Outline each blood parasite and name the species.
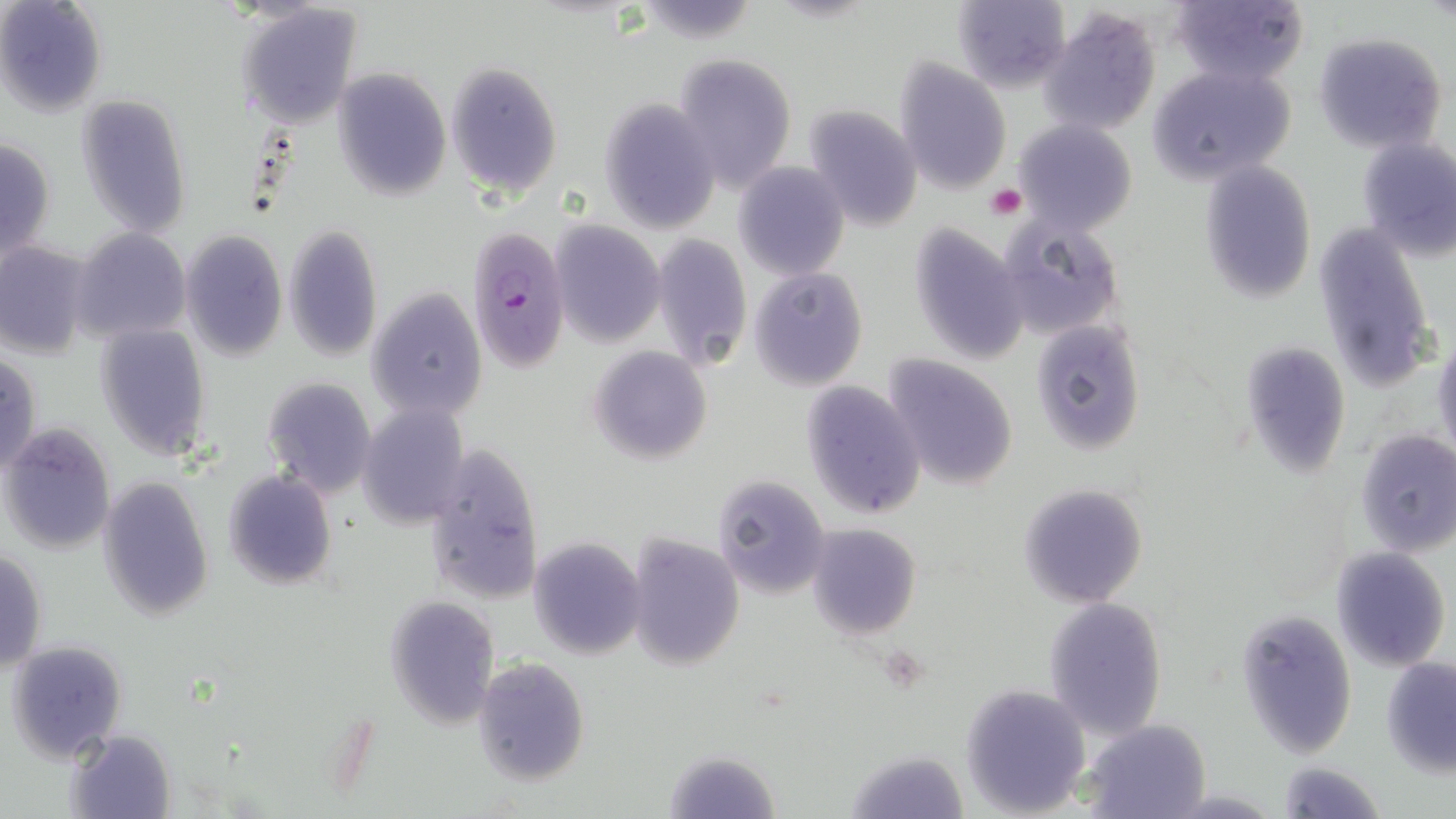

Approximate bounding boxes as (x1, y1, x2, y2) in pixels.
Plasmodium falciparum-infected red blood cells: (465, 223, 572, 370).
No Plasmodium ovale, Plasmodium malariae, Plasmodium vivax, Babesia divergens, or Trypanosoma brucei observed.

slide-level diagnosis = Plasmodium falciparum
field of view = single
preparation = thin blood film
modality = light microscopy
stain = May-Grünwald-Giemsa
uninfected red blood cell locations = approximate bounding boxes as (x1, y1, x2, y2) in pixels: (0, 0, 106, 116), (953, 0, 1071, 94), (1170, 0, 1309, 88), (237, 3, 363, 127), (1040, 9, 1161, 136), (1312, 32, 1447, 152), (673, 53, 797, 192), (894, 60, 1011, 195), (445, 61, 563, 197), (1149, 62, 1299, 185), (331, 68, 450, 201), (75, 96, 191, 237), (599, 100, 723, 233), (802, 106, 922, 229), (1012, 120, 1137, 236), (0, 137, 56, 262), (1356, 137, 1456, 262), (1198, 160, 1318, 305), (734, 163, 850, 280), (1002, 219, 1123, 334), (549, 222, 665, 347), (908, 222, 1030, 366), (1314, 225, 1437, 396), (285, 226, 384, 361), (72, 229, 191, 342), (180, 231, 288, 360), (652, 234, 753, 371), (0, 241, 92, 359), (749, 267, 868, 390), (365, 290, 487, 422), (1028, 321, 1146, 455), (95, 324, 211, 460), (1433, 332, 1456, 464), (1240, 342, 1352, 479), (587, 346, 713, 465), (0, 353, 42, 477), (882, 353, 1019, 490), (261, 376, 376, 499), (800, 380, 926, 521), (360, 402, 471, 527), (1, 424, 116, 555), (1356, 429, 1456, 558), (423, 445, 544, 606), (223, 469, 337, 590), (98, 474, 213, 619), (712, 474, 833, 598), (1017, 483, 1148, 608), (805, 523, 921, 641), (624, 533, 744, 669), (527, 536, 647, 660), (1331, 547, 1451, 670), (0, 549, 48, 673), (386, 597, 498, 730), (1043, 597, 1169, 742), (1234, 609, 1358, 759), (6, 640, 128, 764), (1381, 655, 1456, 776), (473, 657, 590, 786), (960, 683, 1093, 817), (1083, 719, 1211, 819), (68, 728, 176, 818), (845, 745, 969, 817), (665, 748, 779, 819), (1276, 760, 1385, 819)
image size = 1456×819 pixels
magnification = 1000x
platelet locations = approximate bounding boxes as (x1, y1, x2, y2) in pixels: (985, 185, 1026, 220)